Evaluate for malaria.
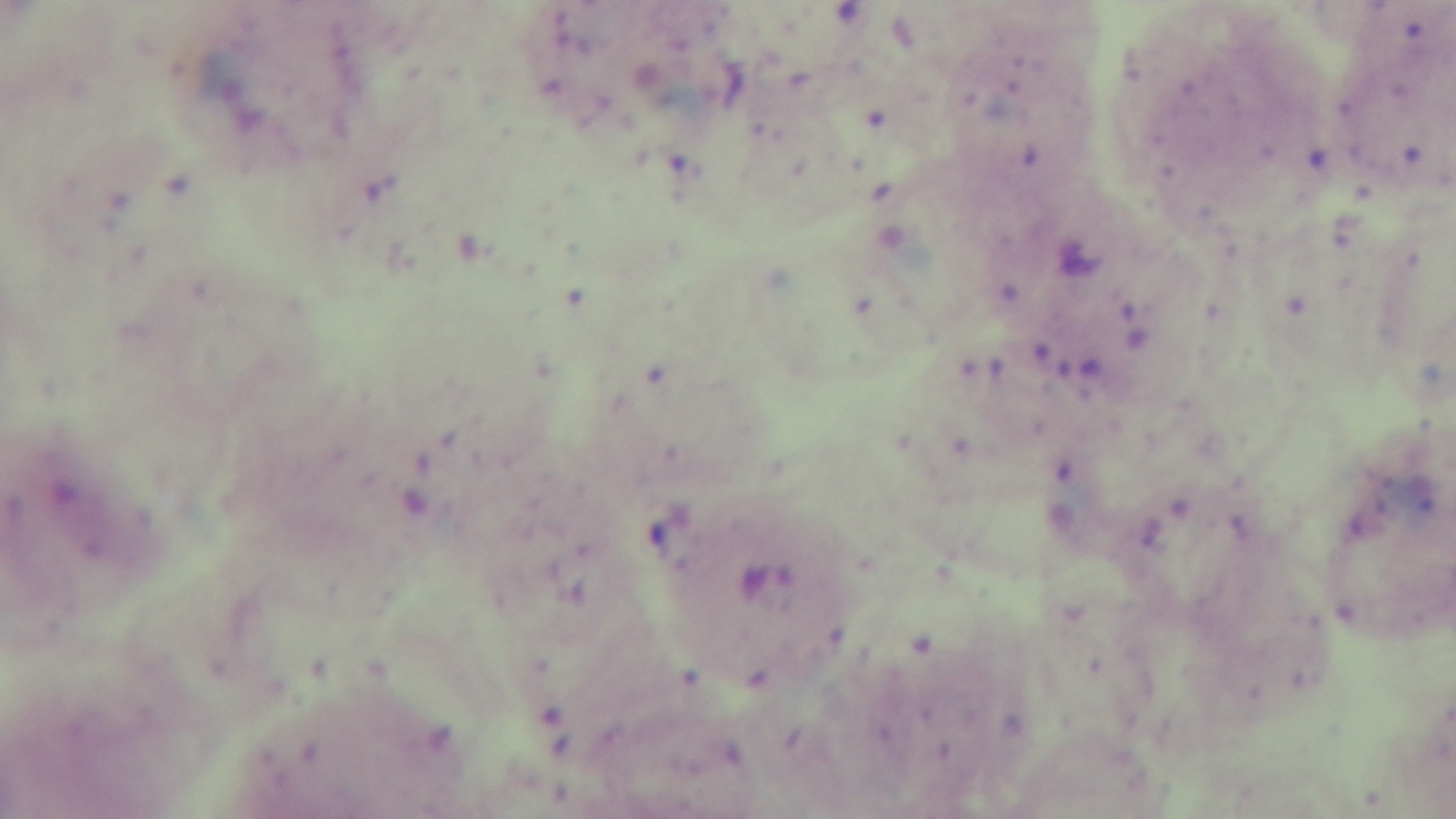

Infected.

Summary:
  - Stain: Giemsa
  - Field of view: single
  - Objective: 100x oil immersion
  - Capture: mounted 4K digital camera
  - Preparation: thick blood film
  - Modality: light microscopy